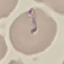
malaria status = uninfected
preparation = thin blood smear
capture = smartphone through the microscope eyepiece
stain = Giemsa
image type = cell patch, automatically extracted from a larger field of view and resized to 64 × 64 pixels